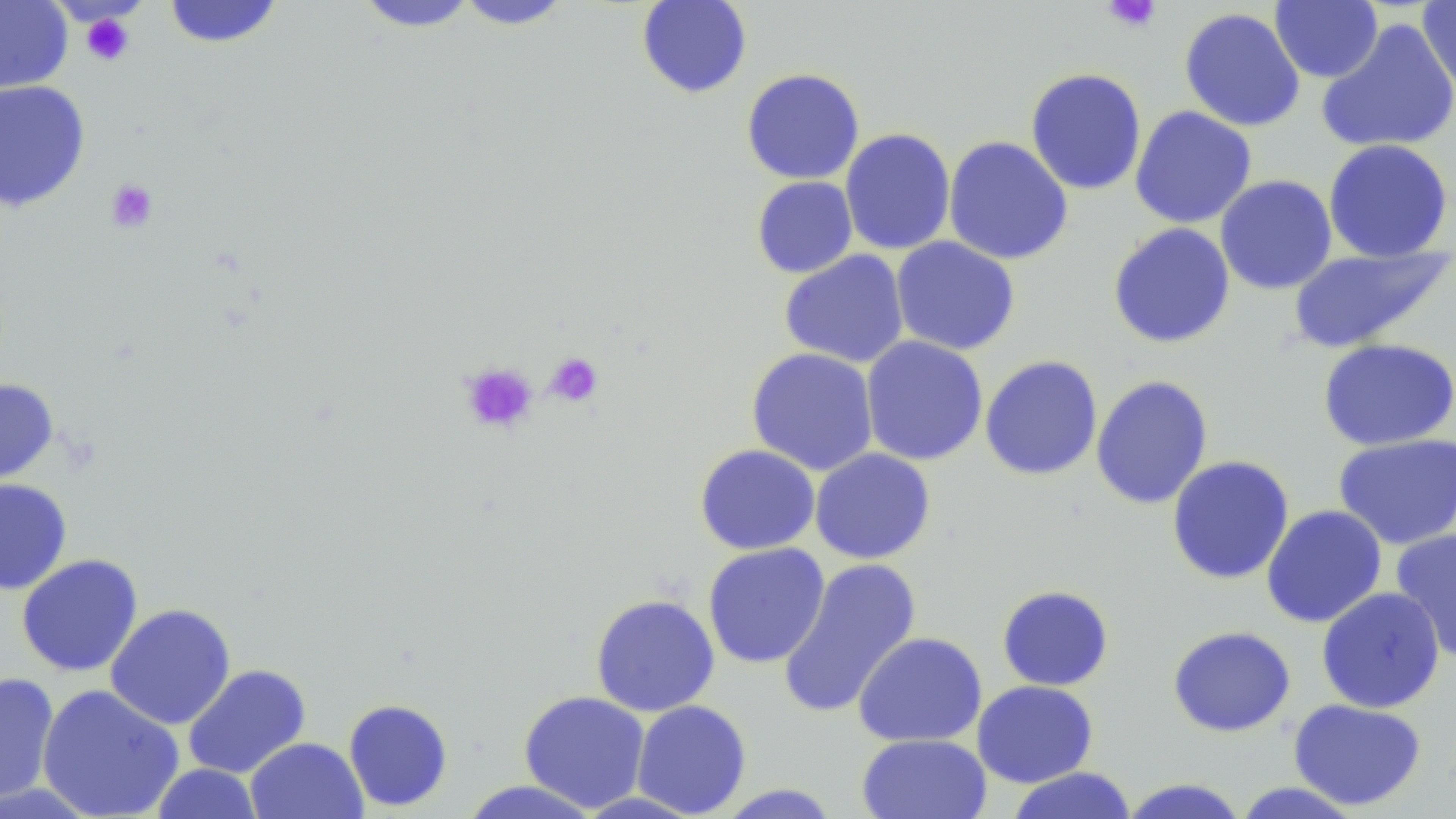 Approximate bounding boxes as (x1,y1)-(x2,y2) corner pairs in pixels. Uninfected red blood cell locations: (0,0)-(73,95), (452,0)-(575,29), (636,0)-(753,98), (1417,0)-(1456,96), (161,1)-(286,49), (353,1)-(481,32), (1270,1)-(1383,83), (1179,6)-(1306,133), (1316,18)-(1456,155), (1025,67)-(1147,195), (740,68)-(865,185), (0,80)-(91,212), (1130,105)-(1257,229), (840,128)-(956,255), (943,136)-(1073,266), (1323,139)-(1454,262), (1215,175)-(1337,295), (751,176)-(858,279), (1108,222)-(1236,349), (891,236)-(1020,356), (1288,244)-(1453,353), (779,249)-(909,368), (861,336)-(988,466), (1317,339)-(1456,451), (746,347)-(879,476), (979,355)-(1103,481), (1090,375)-(1214,510), (0,378)-(59,492), (1333,433)-(1456,550), (694,444)-(821,555), (810,448)-(935,564), (1167,455)-(1294,585), (0,478)-(72,595), (1260,505)-(1387,628), (1390,529)-(1456,662), (702,543)-(830,669), (16,553)-(144,677), (777,559)-(922,719), (996,585)-(1114,691), (1316,586)-(1446,713), (590,594)-(720,717), (106,603)-(236,730), (1167,625)-(1296,737), (852,631)-(987,748), (182,664)-(311,779), (0,672)-(60,805), (972,680)-(1098,788), (36,684)-(185,819), (518,690)-(650,813), (343,698)-(454,812), (1288,699)-(1427,811), (631,700)-(752,817), (856,733)-(992,819), (245,736)-(368,819), (150,763)-(265,818), (1005,767)-(1138,819), (1118,778)-(1250,819), (456,780)-(605,818), (1230,781)-(1366,818), (714,784)-(843,818). Platelet locations: (1101,0)-(1161,33), (80,12)-(136,67), (106,179)-(158,233), (543,352)-(604,407), (459,361)-(539,435). Slide-level diagnosis: negative for blood parasites. Light microscopy. May-Grünwald-Giemsa-stained preparation. Thin blood smear. Single field of view. Image is 1456×819 pixels. Captured at 1000x magnification.